Locate every leukocyte (white blood cell).
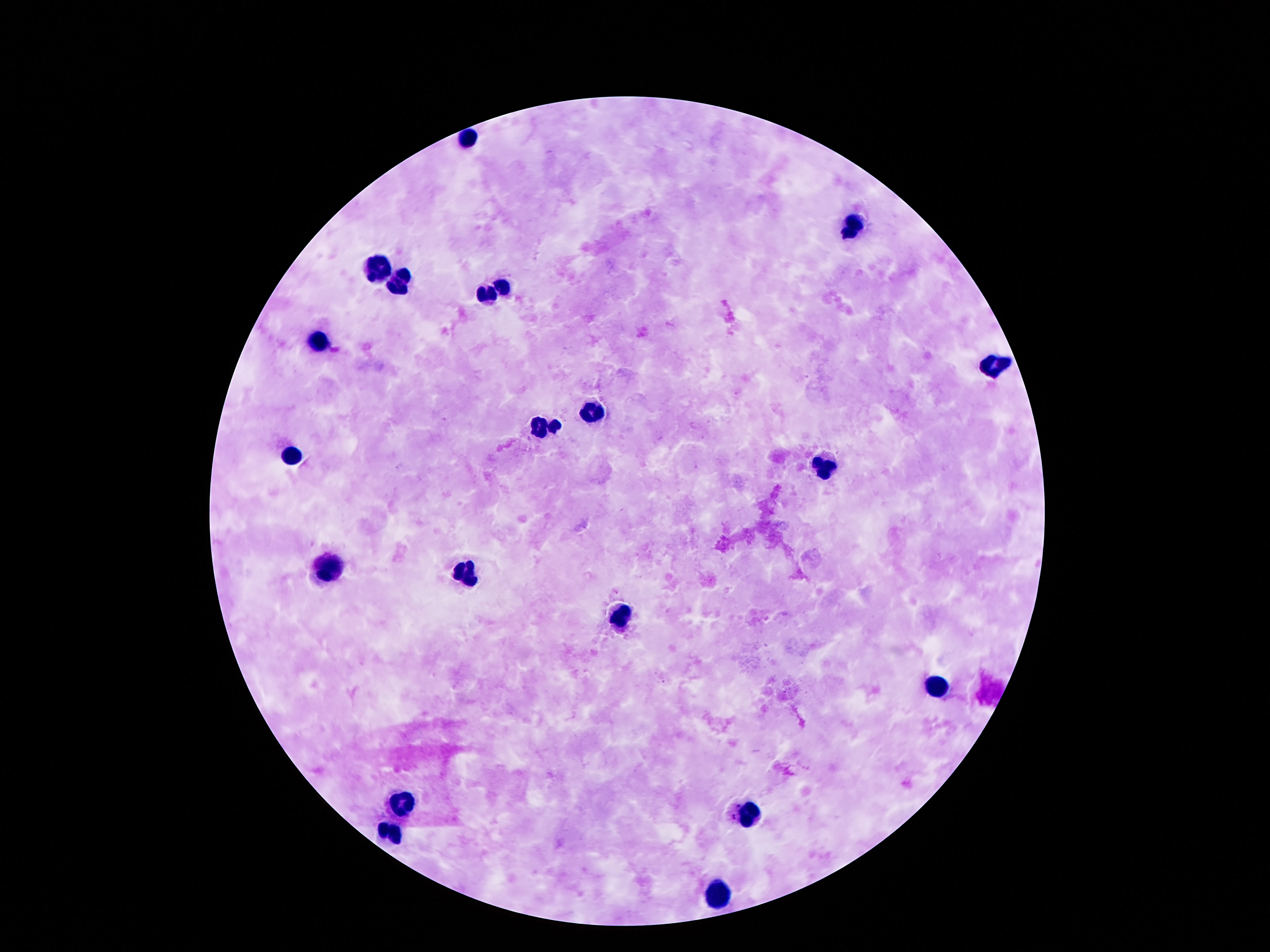
Approximate centers as {x, y} in pixels.
Leukocytes: {471, 133}, {851, 225}, {381, 263}, {397, 281}, {503, 287}, {487, 295}, {321, 340}, {991, 366}, {593, 410}, {545, 425}, {293, 459}, {823, 468}, {327, 570}, {469, 572}, {618, 615}, {935, 688}, {406, 804}, {746, 817}, {389, 829}, {715, 893}.

Summary:
  - Image size: 1270×952 pixels
  - Stain: Giemsa
  - Preparation: thick blood film
  - Patient malaria status: not infected
  - Magnification: 100x
  - Capture: smartphone camera through the microscope eyepiece
  - Field of view: one from this slide